Report the malaria status of this cell.
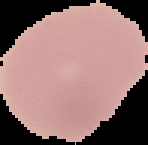
Uninfected.

From a thin blood smear. Image is 148×145 pixels. The area outside the segmented cell region is set to black.